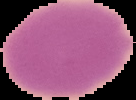

Summary:
  - Malaria status: uninfected
  - Preparation: thin blood smear
  - Image size: 136×100 pixels
  - Image type: segmented cell region with the area outside set to black